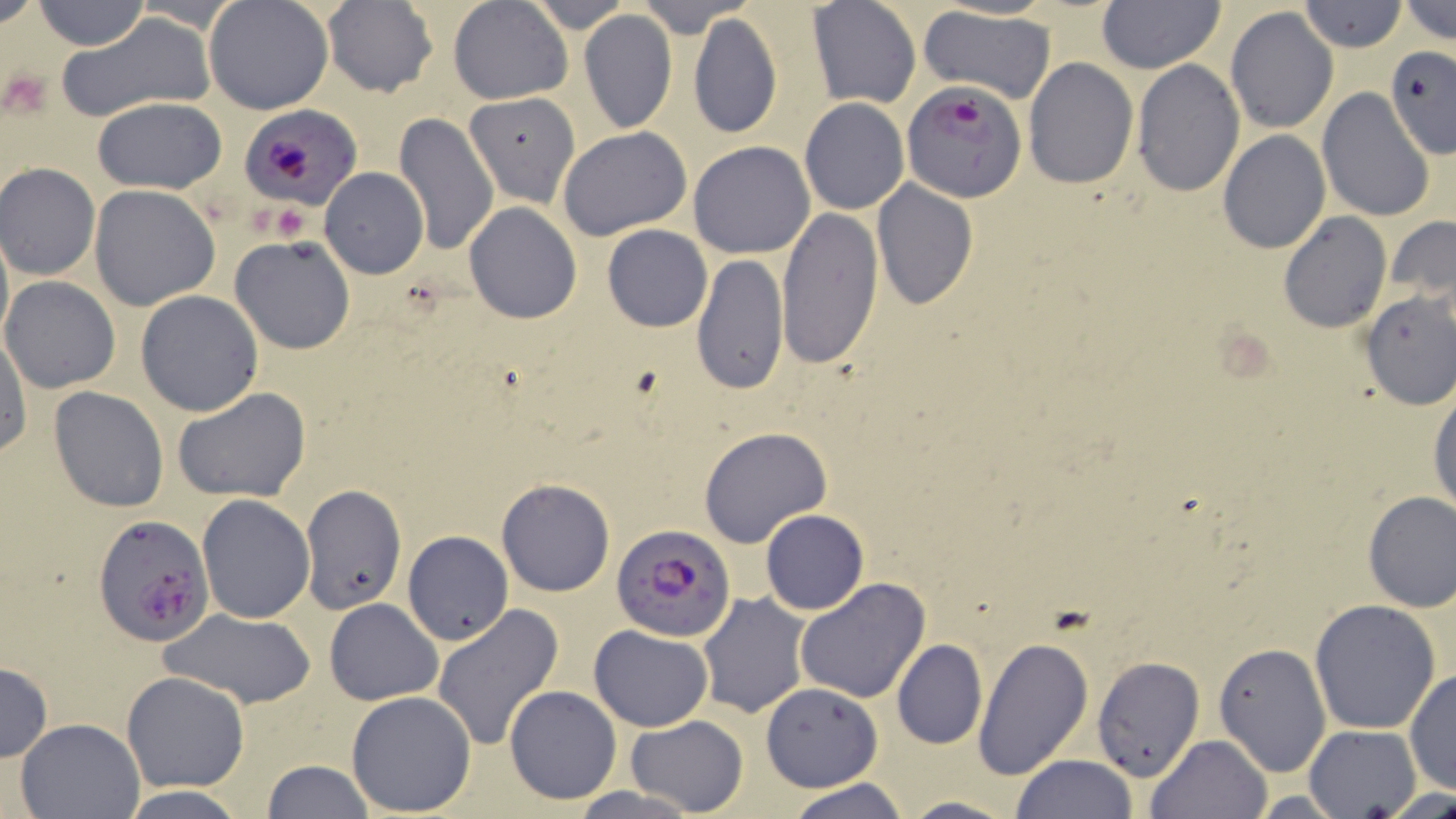

slide-level diagnosis = Plasmodium falciparum
magnification = 1000x
Plasmodium falciparum-infected red blood cell locations = approximate bounding boxes as (x1,y1)-(x2,y2) corner pairs in pixels: (901,80)-(1024,202), (241,106)-(362,211), (92,515)-(213,645), (612,524)-(737,641)
platelet locations = approximate bounding boxes as (x1,y1)-(x2,y2) corner pairs in pixels: (5,70)-(57,117), (269,204)-(307,243)
field of view = one of a larger specimen
uninfected red blood cell locations = approximate bounding boxes as (x1,y1)-(x2,y2) corner pairs in pixels: (32,0)-(148,50), (323,0)-(438,97), (448,0)-(574,104), (525,0)-(636,32), (633,0)-(751,33), (1095,0)-(1226,73), (1398,0)-(1456,46), (204,1)-(333,116), (807,1)-(921,109), (1297,1)-(1407,52), (917,6)-(1055,103), (1225,6)-(1338,135), (579,9)-(677,133), (687,12)-(782,142), (58,13)-(215,124), (1384,44)-(1456,156), (1023,57)-(1138,189), (1132,59)-(1245,196), (1317,88)-(1436,225), (464,91)-(580,207), (91,97)-(227,194), (799,98)-(909,215), (394,111)-(499,257), (556,126)-(693,241), (1216,130)-(1330,254), (687,141)-(815,259), (1,163)-(101,281), (320,168)-(428,278), (871,180)-(979,311), (89,185)-(220,312), (463,202)-(581,323), (774,207)-(884,370), (1279,212)-(1390,333), (1385,216)-(1456,304), (602,224)-(712,331), (229,235)-(356,355), (690,254)-(788,397), (2,276)-(121,393), (136,291)-(264,417), (1358,291)-(1456,409), (1,331)-(31,458), (48,385)-(169,512), (173,388)-(311,503), (1429,389)-(1456,521), (698,426)-(834,549), (496,478)-(615,597), (301,489)-(406,613), (1362,490)-(1456,611), (197,494)-(315,623), (761,509)-(868,614), (403,531)-(514,645), (795,577)-(930,704), (697,592)-(811,719), (324,599)-(444,706), (1309,600)-(1441,735), (431,603)-(564,752), (159,608)-(316,709), (588,624)-(714,732), (971,635)-(1092,780), (891,639)-(987,750), (1213,641)-(1330,777), (1091,653)-(1206,782), (0,661)-(52,760), (1404,667)-(1455,797), (121,671)-(250,792), (758,682)-(881,792), (503,684)-(623,804), (345,690)-(477,813), (624,715)-(747,816), (13,717)-(144,818), (1305,726)-(1423,817), (1146,733)-(1273,819), (1012,754)-(1137,819), (260,760)-(375,817), (784,778)-(913,819), (119,785)-(249,818), (895,795)-(1023,818)
preparation = thin blood film
modality = light microscopy
image size = 1456×819 pixels
stain = May-Grünwald-Giemsa